Comment on the morphology of the red blood cells.
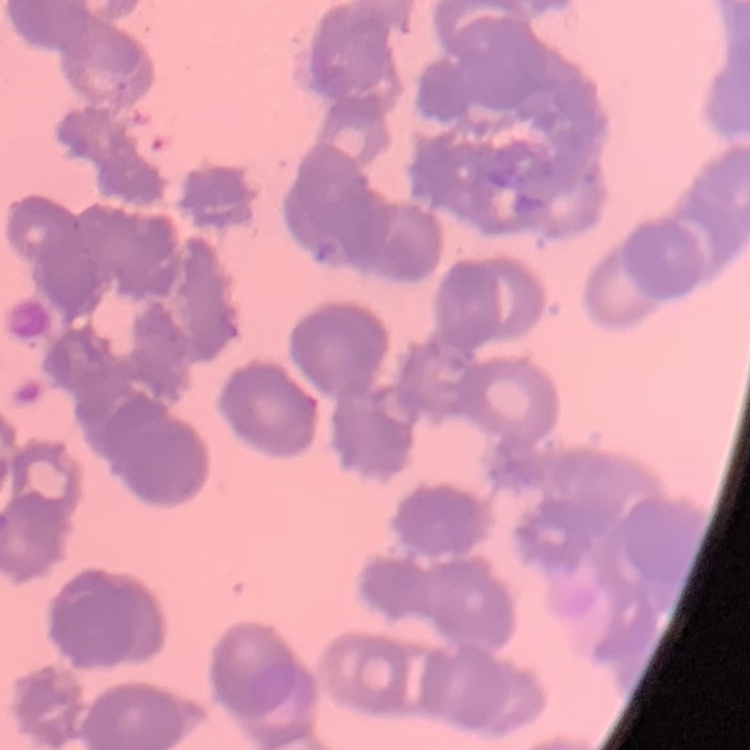

They show rouleaux formation.

Thin blood smear. Square crop of a larger photomicrograph. Stained with either Field's or Giemsa.